State the blood parasite species.
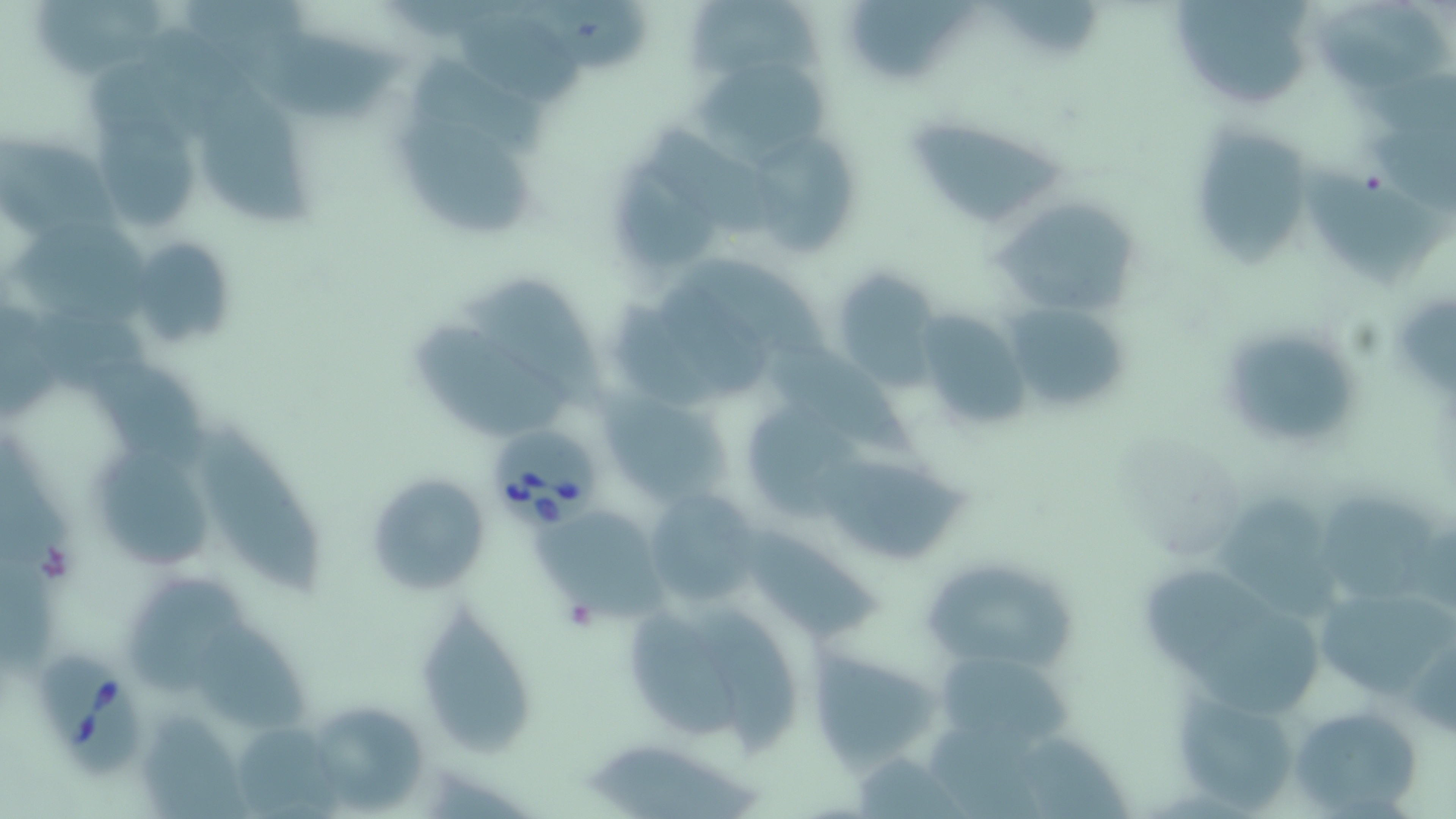

Babesia divergens.

Summary:
  - Coordinate format: approximate bounding boxes as named x1/y1/x2/y2 corners in pixels
  - Uninfected red blood cell locations: (x1=1171, y1=0, x2=1320, y2=110), (x1=692, y1=1, x2=832, y2=77), (x1=854, y1=1, x2=984, y2=76), (x1=1318, y1=2, x2=1455, y2=92), (x1=462, y1=13, x2=587, y2=111), (x1=255, y1=31, x2=410, y2=119), (x1=416, y1=61, x2=549, y2=157), (x1=695, y1=66, x2=834, y2=164), (x1=202, y1=79, x2=318, y2=233), (x1=100, y1=110, x2=201, y2=231), (x1=904, y1=114, x2=1071, y2=227), (x1=396, y1=123, x2=531, y2=236), (x1=645, y1=126, x2=795, y2=236), (x1=1202, y1=128, x2=1313, y2=268), (x1=0, y1=134, x2=142, y2=251), (x1=754, y1=139, x2=858, y2=258), (x1=617, y1=167, x2=720, y2=265), (x1=1309, y1=167, x2=1448, y2=289), (x1=993, y1=196, x2=1142, y2=318), (x1=5, y1=223, x2=156, y2=322), (x1=127, y1=234, x2=239, y2=352), (x1=691, y1=259, x2=828, y2=373), (x1=829, y1=271, x2=944, y2=384), (x1=656, y1=275, x2=774, y2=399), (x1=469, y1=285, x2=610, y2=407), (x1=999, y1=299, x2=1136, y2=417), (x1=618, y1=304, x2=712, y2=405), (x1=913, y1=311, x2=1033, y2=431), (x1=418, y1=325, x2=573, y2=433), (x1=1238, y1=335, x2=1360, y2=440), (x1=773, y1=346, x2=918, y2=454), (x1=88, y1=359, x2=208, y2=473), (x1=605, y1=388, x2=739, y2=516), (x1=200, y1=421, x2=319, y2=590), (x1=102, y1=452, x2=219, y2=570), (x1=821, y1=464, x2=973, y2=564), (x1=364, y1=471, x2=488, y2=595), (x1=643, y1=489, x2=764, y2=604), (x1=1329, y1=493, x2=1443, y2=604), (x1=1221, y1=501, x2=1344, y2=619), (x1=536, y1=517, x2=678, y2=629), (x1=741, y1=528, x2=887, y2=646), (x1=922, y1=557, x2=1076, y2=671), (x1=1143, y1=570, x2=1283, y2=666), (x1=129, y1=579, x2=269, y2=695), (x1=1312, y1=581, x2=1454, y2=705), (x1=614, y1=591, x2=808, y2=751), (x1=422, y1=603, x2=536, y2=756), (x1=1170, y1=612, x2=1324, y2=713), (x1=200, y1=631, x2=312, y2=736), (x1=806, y1=647, x2=942, y2=771), (x1=927, y1=653, x2=1086, y2=754), (x1=1169, y1=684, x2=1301, y2=812), (x1=1288, y1=702, x2=1427, y2=817), (x1=320, y1=710, x2=432, y2=812), (x1=143, y1=720, x2=245, y2=819), (x1=238, y1=720, x2=342, y2=819), (x1=588, y1=741, x2=771, y2=819)
  - Babesia divergens-infected red blood cell locations: (x1=486, y1=425, x2=597, y2=531), (x1=36, y1=649, x2=145, y2=778)
  - Magnification: 1000x
  - Image size: 1456×819 pixels
  - Preparation: thin blood smear
  - Stain: May-Grünwald-Giemsa
  - Field of view: one of a larger specimen
  - Modality: optical microscopy